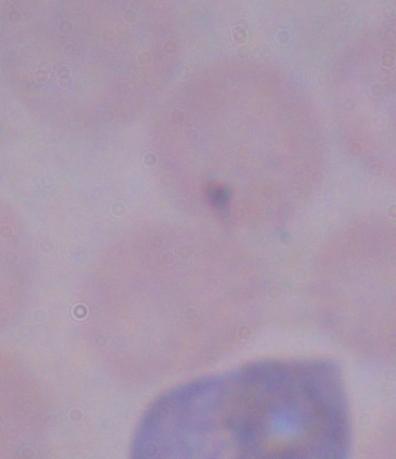

{
  "modality": "photomicrograph",
  "identification": "trypanosome",
  "magnification": "1000x"
}